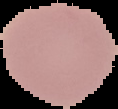

{
  "image_size": "118×109 pixels",
  "malaria_status": "uninfected",
  "image_type": "cell region segmented out of the field of view; surrounding area masked to black",
  "preparation": "thin blood film"
}